Evaluate for Plasmodium parasites.
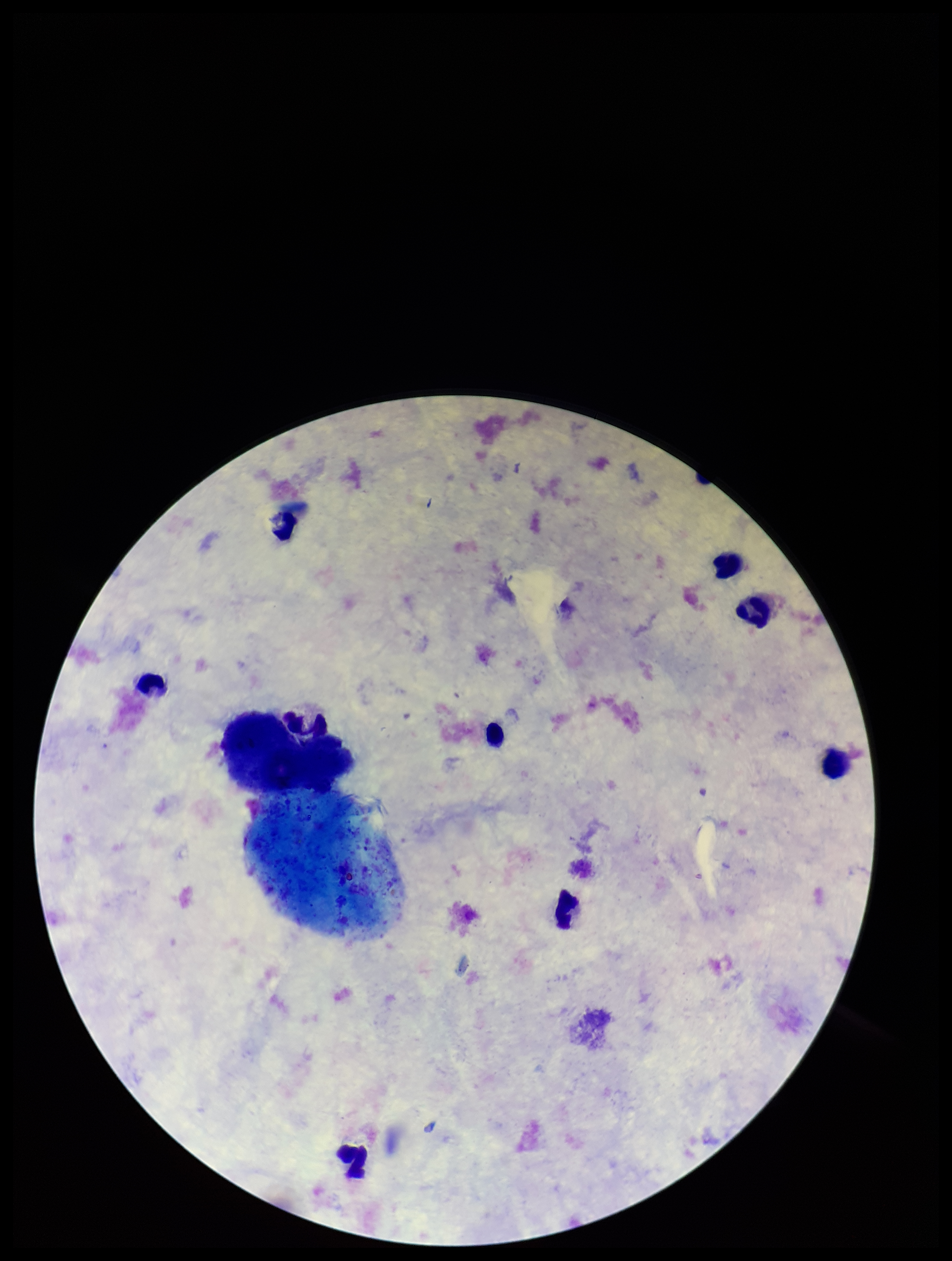
None detected.

Summary:
  - Capture: smartphone photograph through the microscope eyepiece
  - Leukocyte count: 8
  - Preparation: thick blood smear
  - Image size: 952×1261 pixels
  - Field of view: single
  - Patient malaria status: negative
  - Stain: Giemsa
  - Parasite count: 0